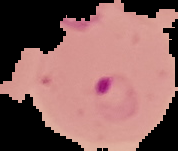

Summary:
  - Preparation: thin blood smear
  - Malaria status: parasitized
  - Image size: 178×151 pixels
  - Image type: cell region segmented out of the field of view; surrounding area masked to black